Report the malaria status of this cell.
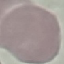
Uninfected.

preparation: thin smear
capture: smartphone camera at the microscope eyepiece
stain: Giemsa
image_type: cell patch, automatically extracted from a larger field of view and resized to 64 × 64 pixels